Assess the morphology of the red blood cells.
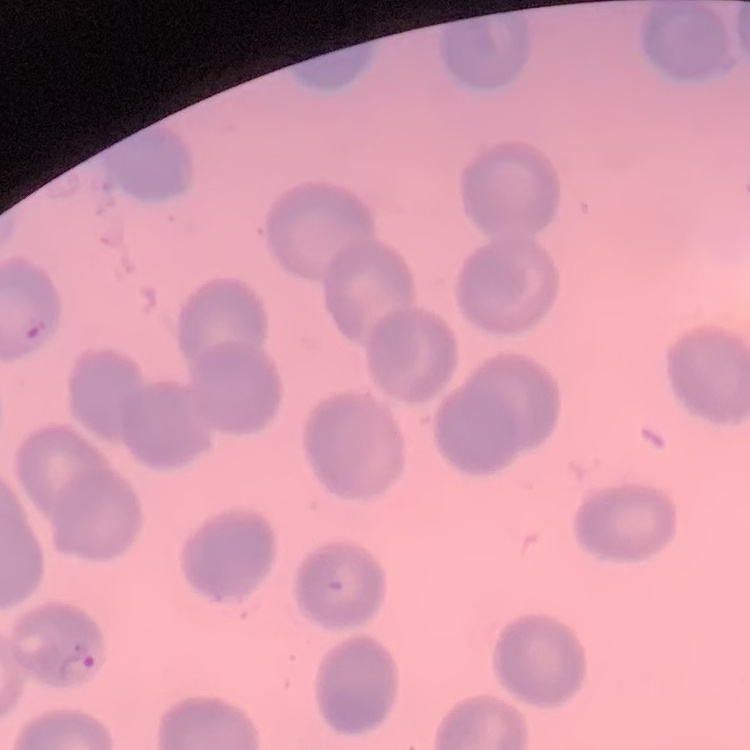

They show no rouleaux formation.

Square crop of a larger photomicrograph. Stained with either Field's or Giemsa. Thin peripheral smear.